Report the malaria status of this cell.
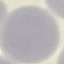
It is uninfected.

preparation: thin smear
image_type: automatically extracted cell patch, resized to 64 × 64 pixels
capture: smartphone camera at the microscope eyepiece
stain: Giemsa